Identify the preparation type.
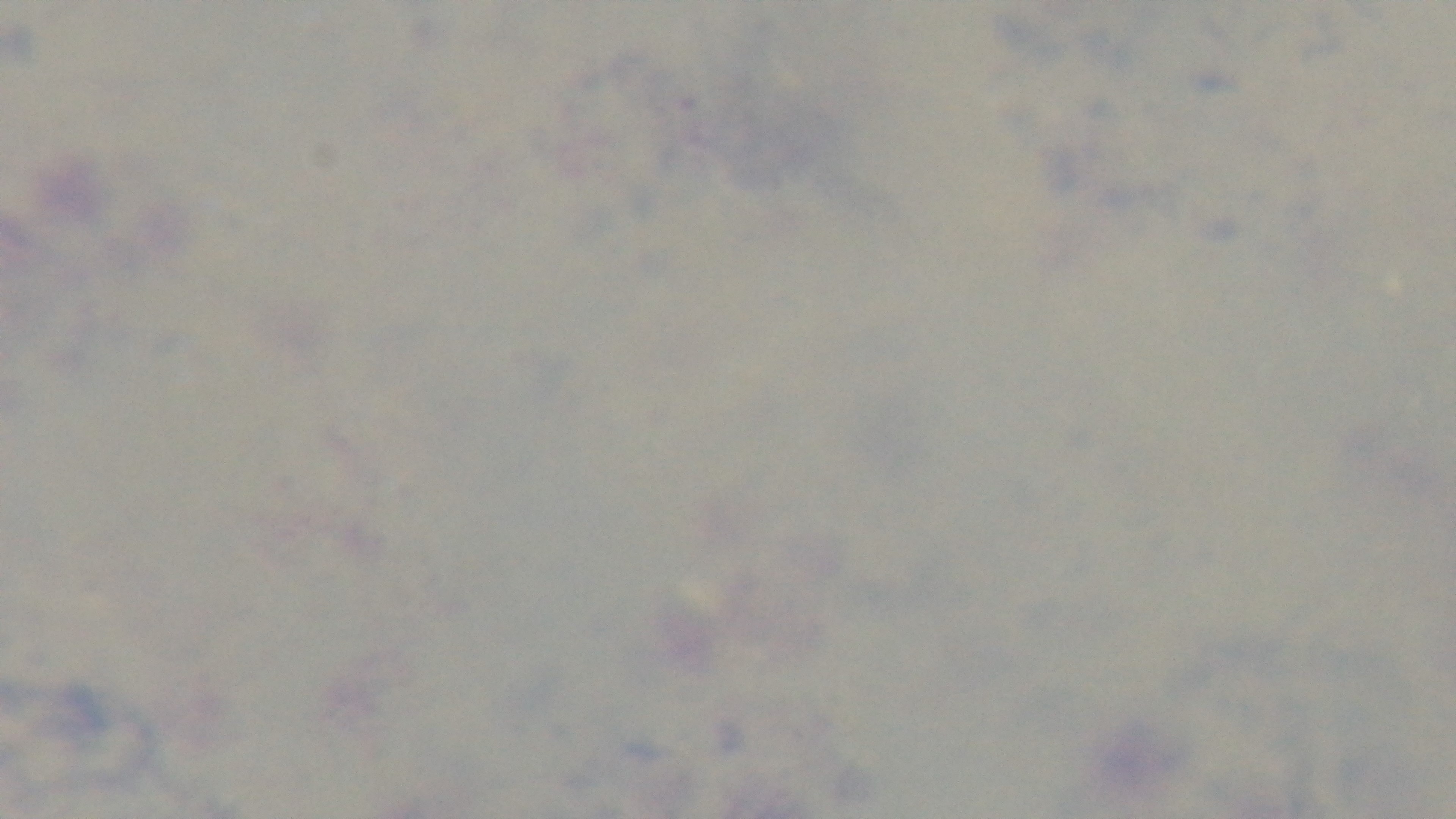
Thick.

Summary:
  - Field of view: one from the slide
  - Malaria status: negative
  - Modality: light microscopy
  - Stain: Giemsa
  - Capture: mounted 4K digital camera
  - Objective: 100x oil immersion